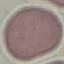
result: no malaria parasites seen
stain: Giemsa
image_type: automatically extracted cell patch, resized to 64 × 64 pixels
preparation: thin smear
capture: smartphone camera at the microscope eyepiece